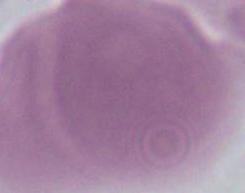

magnification: 1000x
identification: red blood cell
modality: micrograph